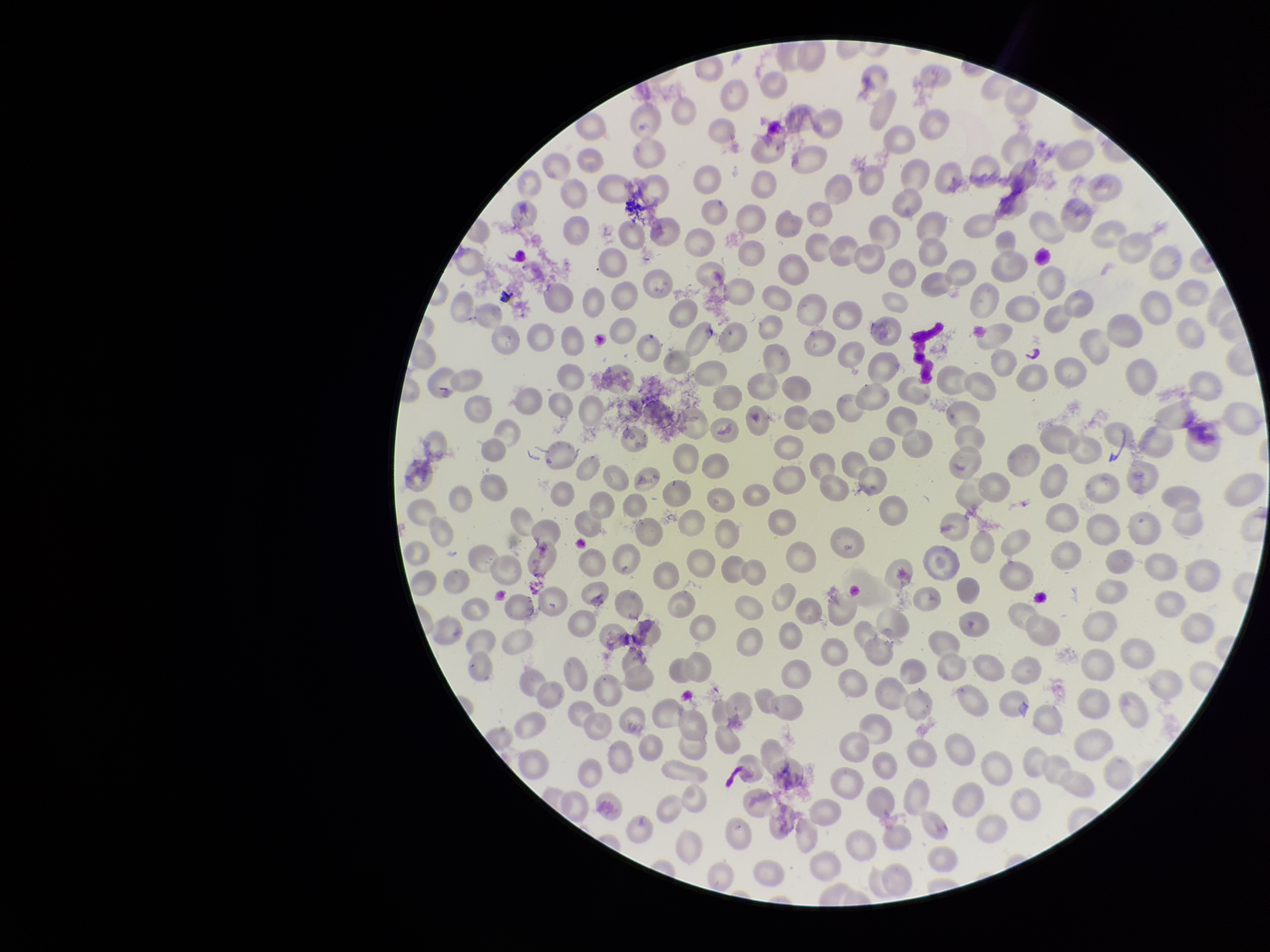

patient_malaria_status: infected
preparation: thin
image_size: 1270×952 pixels
species_reported_for_this_patient: Plasmodium vivax
red_blood_cell_count: 279
field_of_view: one from this slide
capture: smartphone photograph through the microscope eyepiece
parasitized_red_blood_cell_count: 0
stain: Giemsa
parasitized_red_blood_cells: none seen